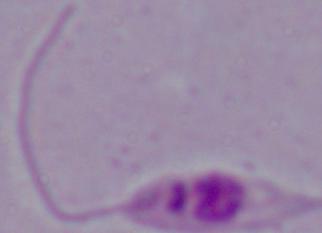
Summary:
  - Magnification: 1000x
  - Identification: Leishmania
  - Modality: micrograph